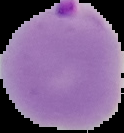

malaria status = parasitized
image size = 124×133 pixels
image type = segmented cell region with the area outside set to black
preparation = thin blood smear